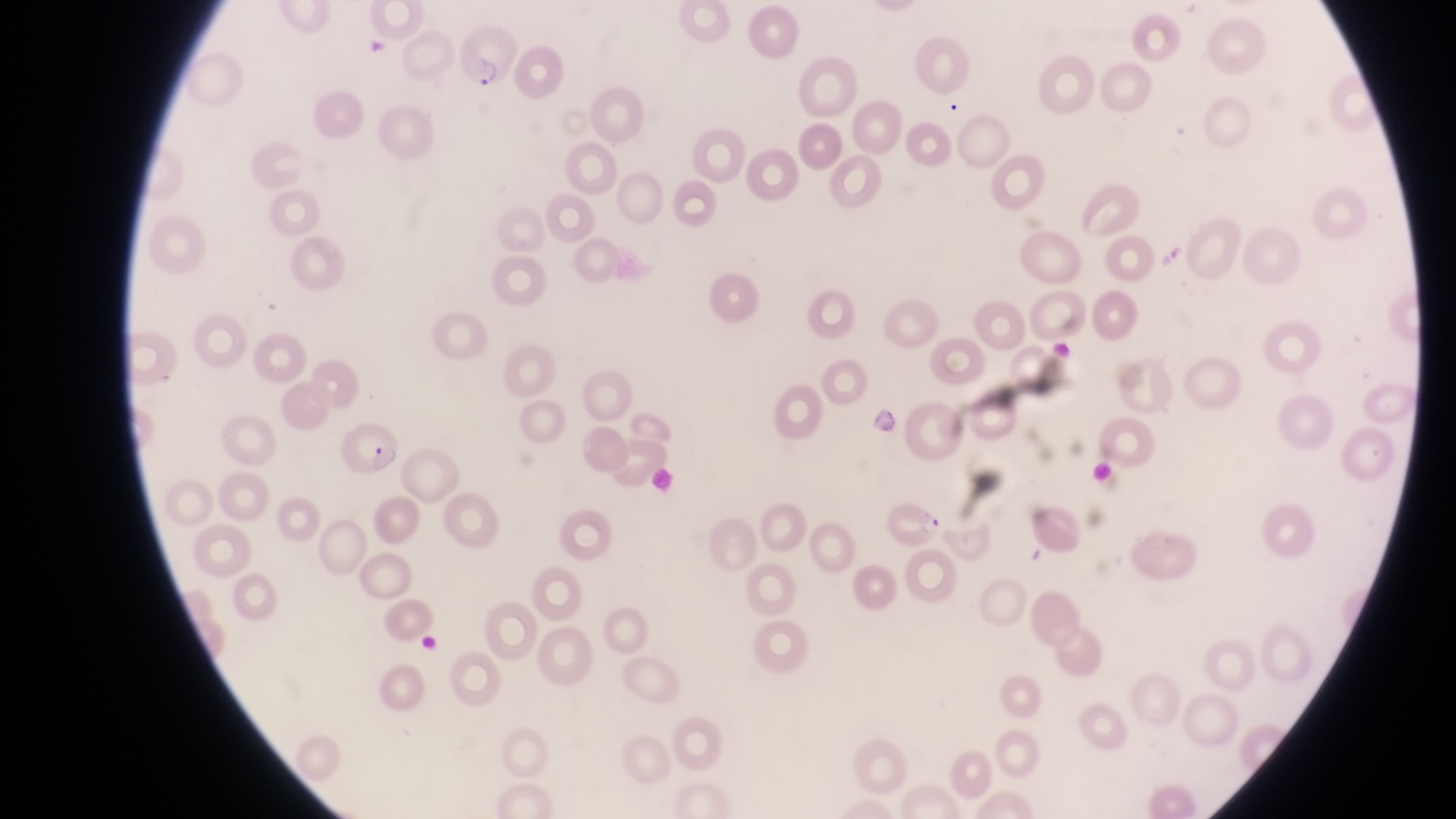

capture = smartphone photograph through the eyepiece of an Olympus CX-23 microscope
field of view = single
preparation = thin blood film
country = Uganda
image size = 1456×819 pixels
parasitised red blood cell locations = approximate bounding boxes as [left, top, right, bottom] in pixels: [455, 26, 516, 93], [346, 410, 404, 474], [885, 497, 945, 549]
magnification = 1000x
artifact (platelet-like body, stain precipitate, or debris) locations = approximate bounding boxes as [left, top, right, bottom] in pixels: [363, 33, 393, 57]